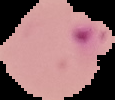

preparation = thin blood film
result = malaria parasites detected
image type = segmented cell region on a black background
image size = 115×100 pixels